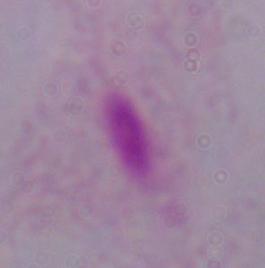
Summary:
  - Modality: micrograph
  - Magnification: 1000x
  - Identification: trichomonad